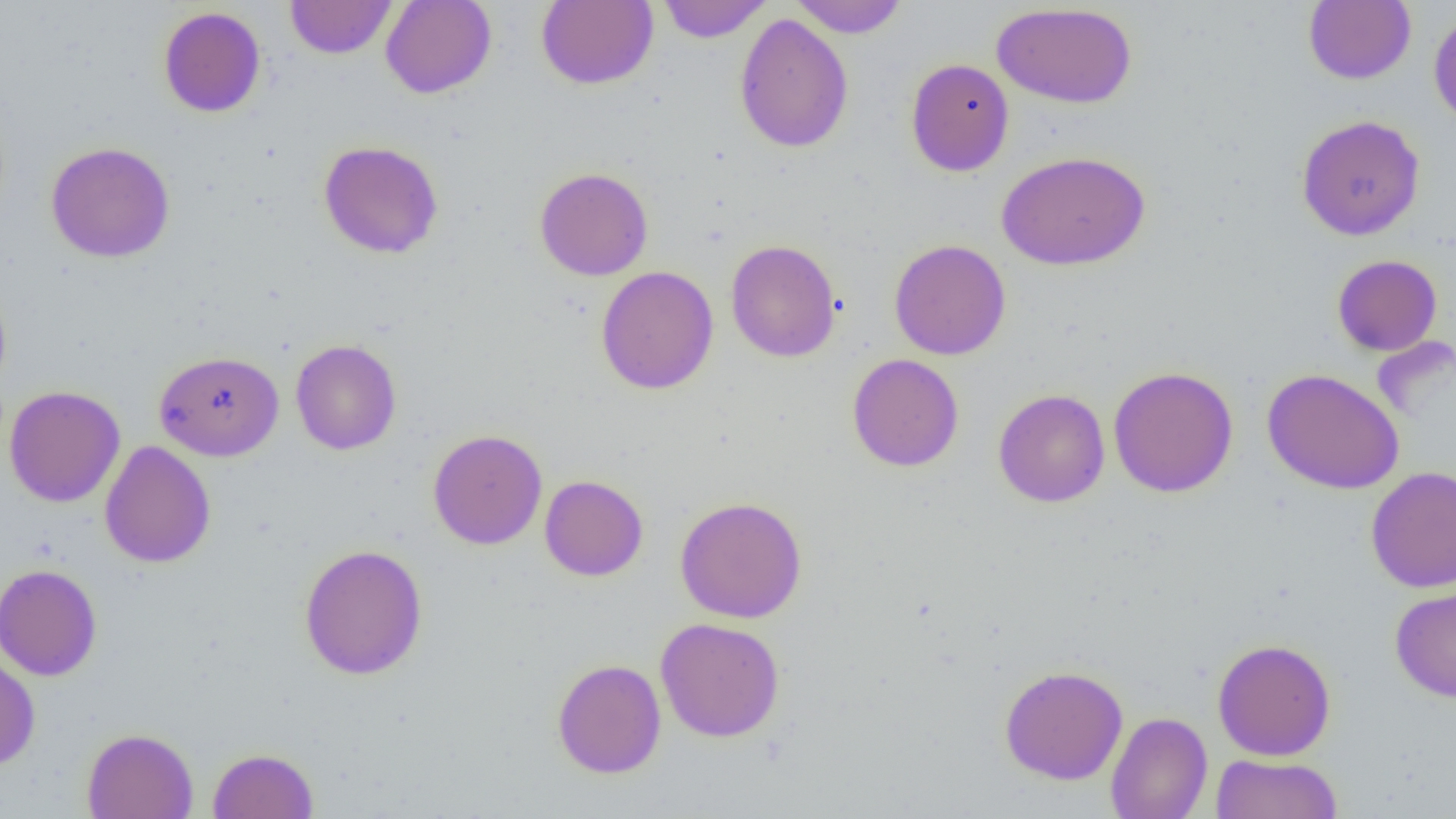
Approximate bounding boxes as named x1/y1/x2/y2 corners in pixels. Uninfected red blood cell locations: (x1=285, y1=0, x2=397, y2=59), (x1=380, y1=0, x2=497, y2=99), (x1=536, y1=0, x2=658, y2=90), (x1=657, y1=0, x2=771, y2=43), (x1=789, y1=0, x2=909, y2=38), (x1=1303, y1=1, x2=1416, y2=85), (x1=991, y1=3, x2=1138, y2=109), (x1=158, y1=6, x2=266, y2=118), (x1=1428, y1=9, x2=1456, y2=128), (x1=734, y1=13, x2=854, y2=153), (x1=905, y1=58, x2=1014, y2=176), (x1=1296, y1=114, x2=1426, y2=241), (x1=318, y1=140, x2=444, y2=259), (x1=46, y1=141, x2=175, y2=263), (x1=996, y1=150, x2=1151, y2=270), (x1=535, y1=167, x2=653, y2=281), (x1=725, y1=239, x2=842, y2=362), (x1=888, y1=239, x2=1011, y2=361), (x1=1331, y1=254, x2=1443, y2=356), (x1=595, y1=266, x2=719, y2=394), (x1=0, y1=279, x2=12, y2=397), (x1=290, y1=338, x2=402, y2=455), (x1=153, y1=350, x2=284, y2=461), (x1=846, y1=353, x2=964, y2=472), (x1=1108, y1=366, x2=1239, y2=498), (x1=1262, y1=368, x2=1404, y2=495), (x1=4, y1=385, x2=125, y2=507), (x1=993, y1=389, x2=1110, y2=507), (x1=428, y1=429, x2=547, y2=550), (x1=99, y1=440, x2=216, y2=568), (x1=1366, y1=466, x2=1456, y2=593), (x1=539, y1=475, x2=648, y2=581), (x1=675, y1=496, x2=808, y2=623), (x1=298, y1=543, x2=429, y2=680), (x1=0, y1=563, x2=102, y2=681), (x1=1389, y1=582, x2=1456, y2=702), (x1=655, y1=617, x2=785, y2=742), (x1=1213, y1=638, x2=1336, y2=761), (x1=0, y1=653, x2=40, y2=770), (x1=551, y1=658, x2=666, y2=779), (x1=999, y1=664, x2=1128, y2=785), (x1=1105, y1=711, x2=1212, y2=819), (x1=81, y1=728, x2=198, y2=819), (x1=207, y1=747, x2=319, y2=819), (x1=1210, y1=753, x2=1343, y2=818). Slide-level diagnosis: negative for blood parasites. 1000x magnification. Single field of view. Optical microscopy. Thin blood smear. Image is 1456×819 pixels.